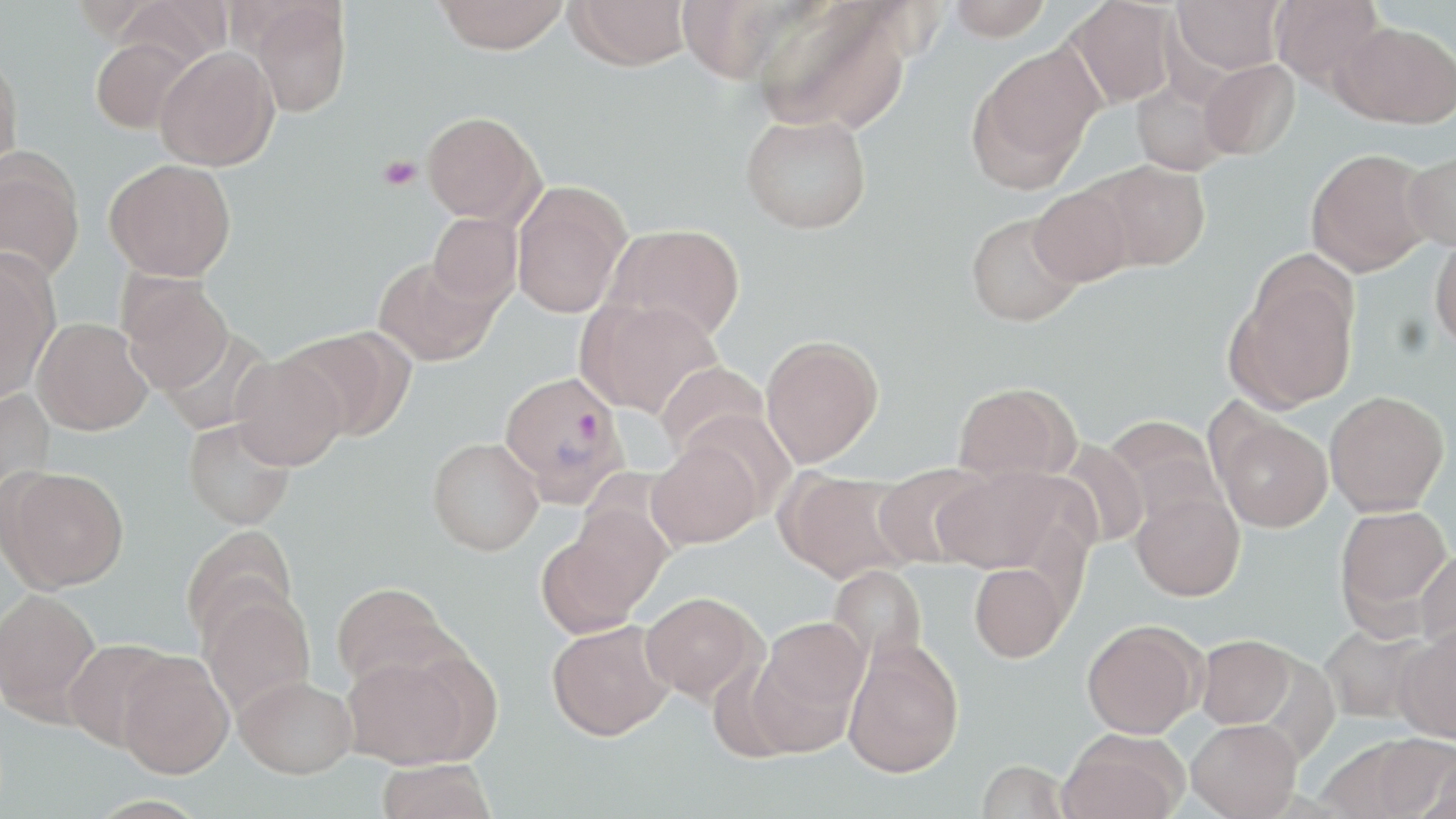

Approximate bounding boxes as [x1, y1, x2, y2] in pixels. Platelet locations: [378, 155, 420, 190]. Uninfected red blood cell locations: [109, 0, 230, 74], [434, 0, 569, 54], [567, 0, 691, 70], [946, 0, 1053, 41], [1065, 0, 1176, 108], [1172, 0, 1286, 74], [1270, 0, 1385, 88], [245, 2, 353, 118], [753, 2, 911, 134], [1335, 20, 1456, 128], [90, 37, 196, 134], [155, 46, 279, 171], [968, 46, 1102, 189], [0, 52, 24, 175], [1198, 59, 1300, 161], [1131, 78, 1234, 175], [422, 111, 544, 225], [741, 112, 872, 234], [0, 147, 86, 281], [1306, 148, 1435, 276], [1402, 149, 1456, 251], [105, 158, 237, 281], [1087, 159, 1210, 271], [511, 180, 631, 318], [1029, 186, 1135, 287], [966, 211, 1083, 327], [427, 212, 523, 309], [604, 223, 745, 342], [1430, 233, 1456, 352], [0, 251, 59, 402], [373, 257, 499, 367], [1228, 267, 1359, 411], [118, 272, 234, 394], [578, 297, 723, 419], [32, 317, 152, 435], [287, 327, 416, 441], [159, 328, 275, 436], [760, 335, 884, 468], [230, 353, 347, 471], [655, 361, 771, 463], [953, 382, 1078, 483], [0, 388, 56, 509], [1324, 391, 1449, 516], [1211, 411, 1333, 532], [1102, 415, 1224, 532], [183, 417, 296, 530], [427, 437, 544, 556], [648, 438, 762, 547], [1057, 441, 1149, 549], [872, 463, 991, 568], [2, 466, 129, 591], [932, 466, 1076, 575], [777, 468, 914, 584], [1131, 490, 1245, 601], [1335, 505, 1453, 624], [543, 511, 667, 633], [181, 525, 299, 647], [1415, 550, 1456, 653], [969, 563, 1069, 662], [828, 564, 927, 669], [331, 581, 454, 689], [0, 588, 101, 721], [199, 588, 316, 717], [641, 591, 764, 705], [749, 617, 869, 752], [546, 620, 674, 740], [1082, 620, 1204, 738], [1320, 624, 1433, 724], [1395, 626, 1456, 742], [1196, 635, 1296, 728], [62, 639, 178, 750], [843, 639, 964, 777], [340, 647, 484, 769], [117, 651, 235, 778], [235, 675, 356, 778], [1187, 718, 1301, 818], [1058, 729, 1188, 819], [1367, 734, 1456, 817], [1420, 747, 1455, 819], [377, 759, 496, 819], [976, 760, 1071, 818]. Plasmodium vivax-infected red blood cell locations: [499, 370, 631, 507]. Slide-level diagnosis: Plasmodium vivax. Image is 1456×819 pixels. Optical microscopy. Captured at 1000x magnification. Thin blood film. One field of a larger specimen. May-Grünwald-Giemsa stain.